Identify the parasite.
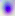
This is Toxoplasma gondii.

Photomicrograph. Captured at 400x magnification.